Classify this cell by malaria status.
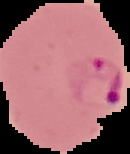
Parasitized.

Cell region segmented out of the field of view; the surrounding area is masked to black. From a thin blood film. Image is 130×154 pixels.